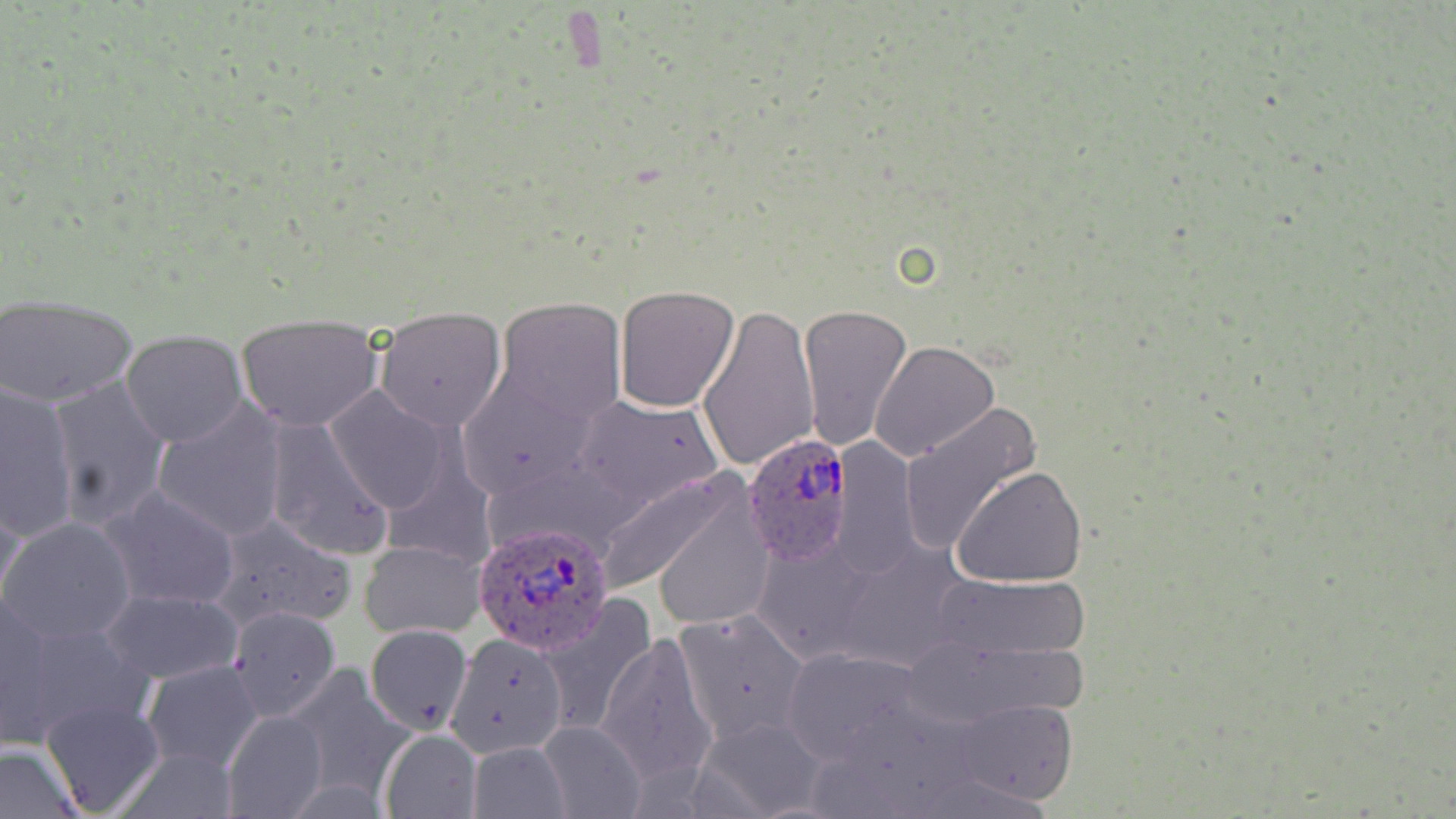

slide-level diagnosis = Plasmodium ovale
magnification = 1000x
image size = 1456×819 pixels
Plasmodium ovale-infected red blood cell locations = approximate bounding boxes as named x1/y1/x2/y2 corners in pixels: (x1=742, y1=435, x2=852, y2=569), (x1=473, y1=524, x2=617, y2=656)
preparation = thin blood film
modality = light microscopy
stain = May-Grünwald-Giemsa
field of view = single
uninfected red blood cell locations = approximate bounding boxes as named x1/y1/x2/y2 corners in pixels: (x1=614, y1=285, x2=741, y2=412), (x1=0, y1=295, x2=138, y2=406), (x1=495, y1=297, x2=628, y2=424), (x1=698, y1=302, x2=819, y2=474), (x1=798, y1=302, x2=913, y2=451), (x1=375, y1=306, x2=507, y2=429), (x1=236, y1=315, x2=383, y2=431), (x1=121, y1=330, x2=248, y2=446), (x1=871, y1=341, x2=1000, y2=462), (x1=454, y1=371, x2=598, y2=498), (x1=47, y1=377, x2=172, y2=533), (x1=0, y1=378, x2=79, y2=540), (x1=326, y1=388, x2=454, y2=515), (x1=570, y1=393, x2=723, y2=512), (x1=152, y1=400, x2=288, y2=541), (x1=899, y1=401, x2=1041, y2=556), (x1=265, y1=418, x2=393, y2=561), (x1=834, y1=438, x2=924, y2=579), (x1=953, y1=465, x2=1088, y2=587), (x1=591, y1=466, x2=760, y2=601), (x1=0, y1=482, x2=27, y2=615), (x1=102, y1=486, x2=241, y2=612), (x1=653, y1=497, x2=775, y2=630), (x1=210, y1=514, x2=358, y2=632), (x1=2, y1=517, x2=136, y2=646), (x1=753, y1=536, x2=873, y2=666), (x1=359, y1=540, x2=486, y2=640), (x1=830, y1=543, x2=971, y2=674), (x1=933, y1=574, x2=1090, y2=662), (x1=102, y1=587, x2=244, y2=682), (x1=0, y1=589, x2=55, y2=746), (x1=538, y1=598, x2=658, y2=745), (x1=228, y1=606, x2=341, y2=720), (x1=673, y1=606, x2=810, y2=745), (x1=9, y1=610, x2=152, y2=745), (x1=366, y1=622, x2=473, y2=737), (x1=597, y1=631, x2=719, y2=788), (x1=449, y1=635, x2=571, y2=760), (x1=782, y1=648, x2=930, y2=765), (x1=141, y1=659, x2=265, y2=773), (x1=282, y1=666, x2=415, y2=804), (x1=38, y1=695, x2=166, y2=818), (x1=947, y1=700, x2=1078, y2=806), (x1=224, y1=709, x2=327, y2=819), (x1=698, y1=715, x2=832, y2=818), (x1=539, y1=718, x2=647, y2=819), (x1=380, y1=729, x2=482, y2=818), (x1=467, y1=740, x2=572, y2=818), (x1=0, y1=742, x2=81, y2=817)